Locate every blood parasite and identify its species.
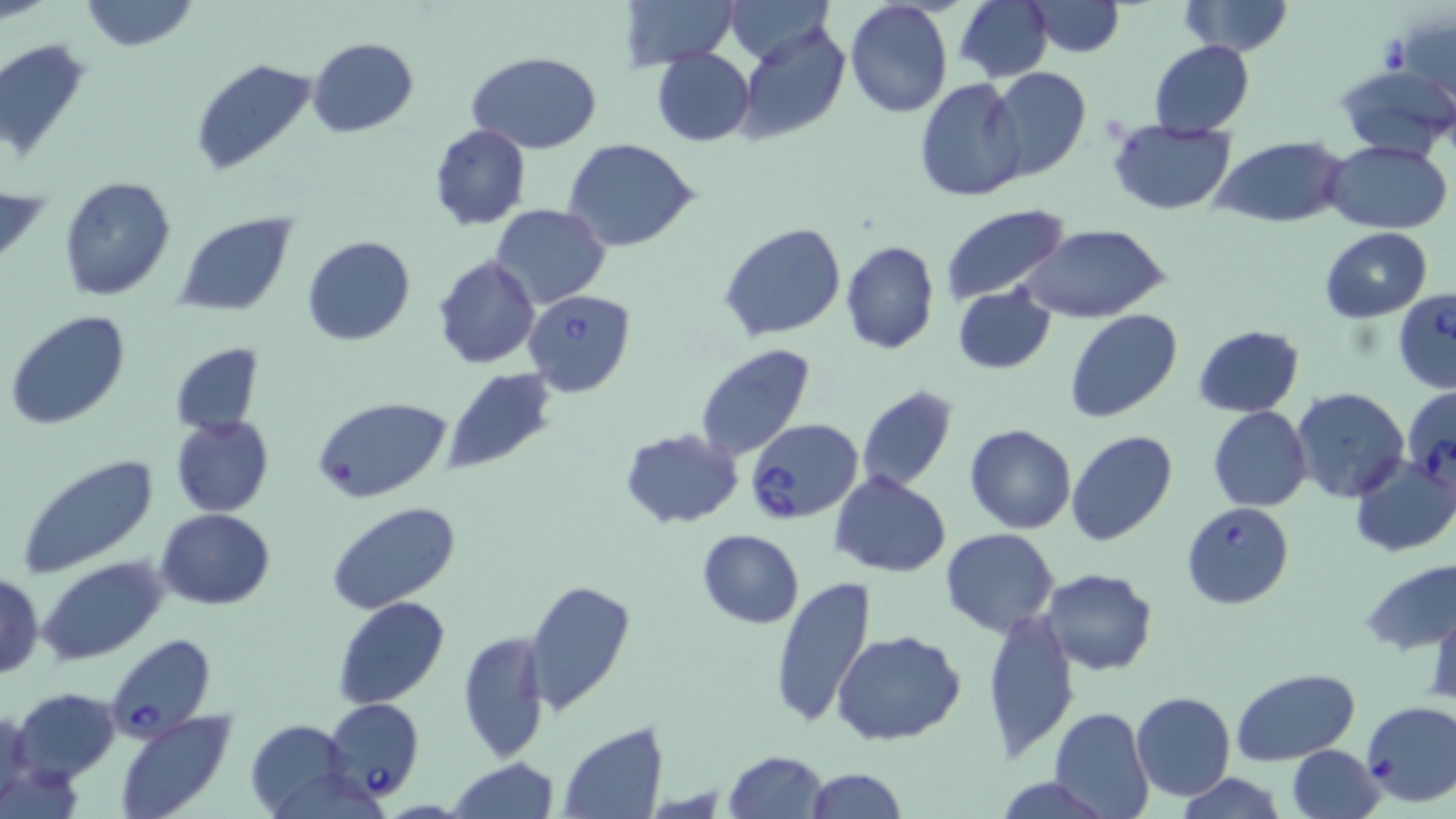

Approximate bounding boxes as (x1, y1, x2, y2) in pixels.
Babesia divergens-infected red blood cells: (523, 289, 636, 397), (1393, 290, 1456, 394), (1402, 384, 1456, 488), (746, 419, 864, 524), (1180, 501, 1296, 609), (106, 634, 218, 740), (323, 698, 424, 801).
No Plasmodium falciparum, Plasmodium ovale, Plasmodium malariae, Plasmodium vivax, or Trypanosoma brucei observed.

Summary:
  - Uninfected red blood cell locations: (79, 0, 200, 53), (619, 0, 739, 70), (723, 0, 834, 65), (954, 0, 1052, 83), (1023, 1, 1127, 58), (1177, 1, 1294, 56), (843, 2, 953, 118), (1392, 17, 1454, 108), (738, 24, 852, 145), (308, 36, 418, 137), (0, 38, 92, 164), (1149, 40, 1256, 137), (651, 48, 757, 147), (466, 51, 602, 155), (190, 57, 317, 176), (1333, 64, 1456, 161), (987, 69, 1091, 182), (915, 78, 1028, 203), (1108, 120, 1239, 214), (428, 125, 531, 230), (1212, 137, 1350, 229), (562, 139, 701, 253), (1328, 141, 1452, 232), (59, 176, 176, 301), (490, 203, 610, 309), (939, 203, 1071, 306), (173, 212, 297, 315), (719, 221, 847, 343), (1018, 223, 1172, 325), (1319, 227, 1433, 323), (301, 235, 415, 346), (839, 241, 940, 354), (432, 255, 541, 368), (952, 286, 1057, 374), (1064, 309, 1182, 424), (6, 310, 130, 430), (1191, 324, 1305, 417), (169, 342, 262, 436), (695, 343, 817, 462), (441, 368, 556, 474), (855, 385, 958, 493), (1289, 387, 1411, 503), (312, 395, 453, 503), (1207, 406, 1312, 512), (171, 415, 275, 517), (964, 423, 1077, 533), (619, 429, 744, 527), (1065, 430, 1178, 546), (1348, 450, 1456, 558), (12, 454, 158, 579), (830, 472, 952, 578), (325, 502, 462, 615), (155, 508, 276, 609), (941, 528, 1061, 638), (696, 529, 805, 629), (39, 557, 167, 664), (1359, 557, 1456, 655), (1041, 567, 1158, 675), (1, 572, 44, 678), (769, 576, 878, 731), (521, 577, 635, 716), (332, 595, 450, 710), (1428, 603, 1456, 707), (982, 606, 1079, 761), (833, 630, 966, 746), (458, 631, 549, 762), (1231, 667, 1359, 764), (12, 687, 121, 782), (1131, 691, 1237, 801), (1361, 700, 1456, 807), (0, 706, 35, 815), (1048, 706, 1154, 819), (114, 711, 236, 819), (245, 718, 354, 818), (558, 723, 668, 818), (1285, 744, 1384, 818), (724, 749, 827, 818), (446, 758, 560, 818), (803, 767, 906, 819), (1175, 772, 1287, 819), (992, 775, 1108, 817)
  - Slide-level diagnosis: Babesia divergens
  - Stain: May-Grünwald-Giemsa
  - Magnification: 1000x
  - Field of view: one of a larger specimen
  - Image size: 1456×819 pixels
  - Preparation: thin blood smear
  - Modality: light microscopy